Comment on the morphology of the erythrocytes.
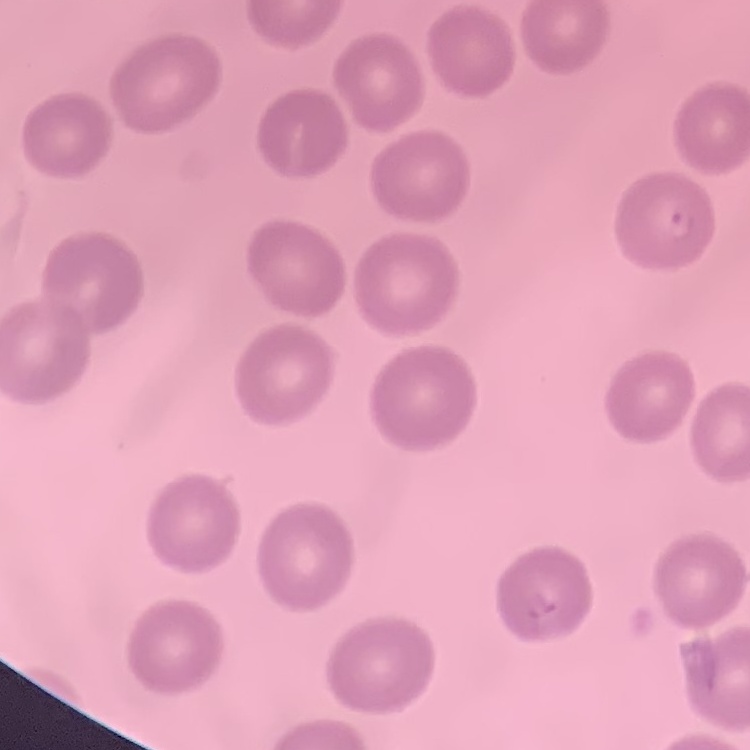
They show no rouleaux formation.

stain = Field's or Giemsa
preparation = thin peripheral smear
image type = one tile cut from a larger photomicrograph